Identify the cell.
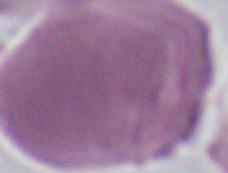
This is an erythrocyte.

{
  "modality": "photomicrograph",
  "magnification": "1000x"
}